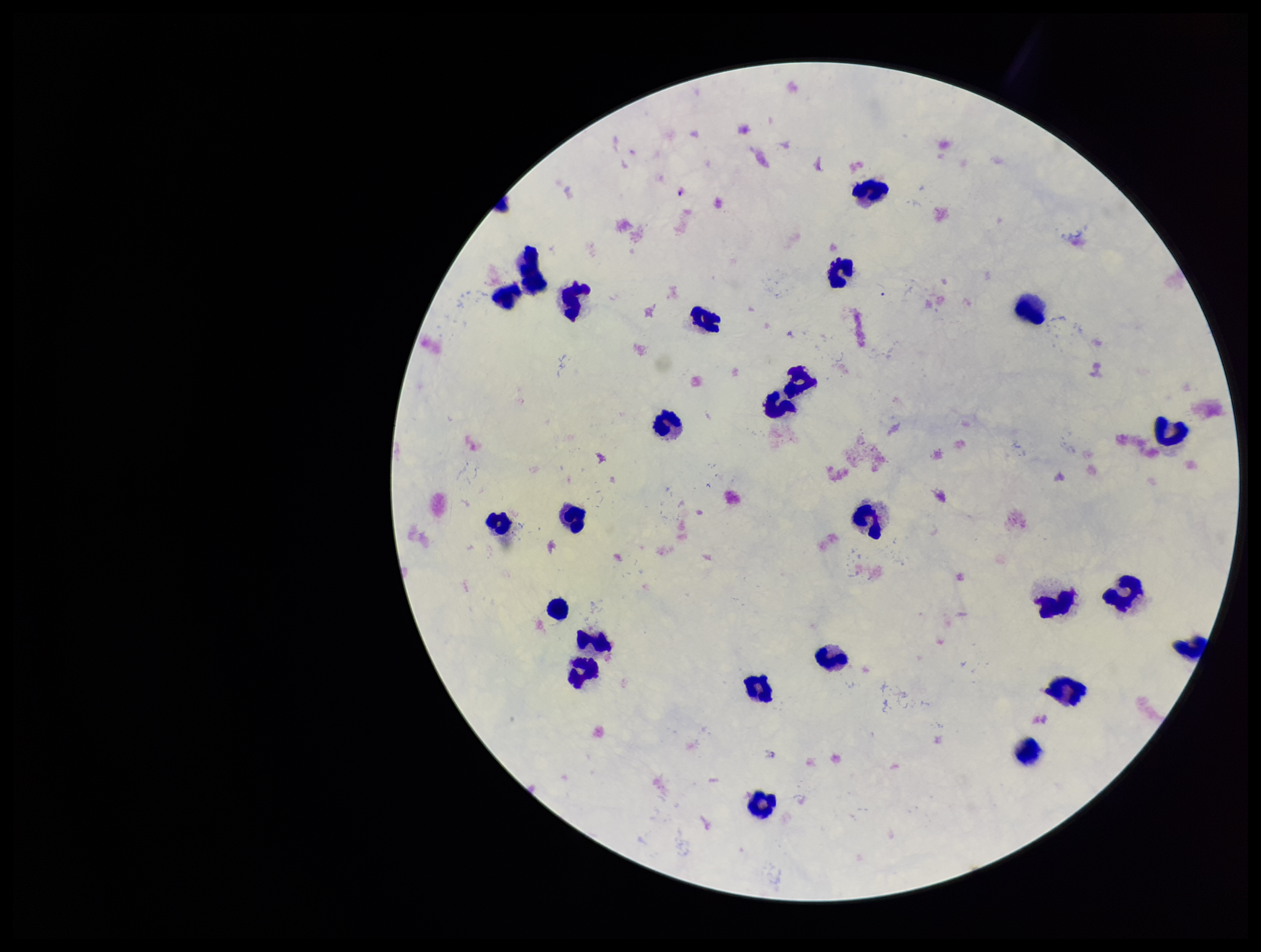

Image is 1261×952 pixels. Giemsa stain. Photographed through the microscope eyepiece with a smartphone camera. Plasmodium parasites: none seen. Preparation: thick blood smear. Leukocyte count: 26. One field from this slide. Patient malaria status: negative. Parasite count: 0.